Name the parasite shown.
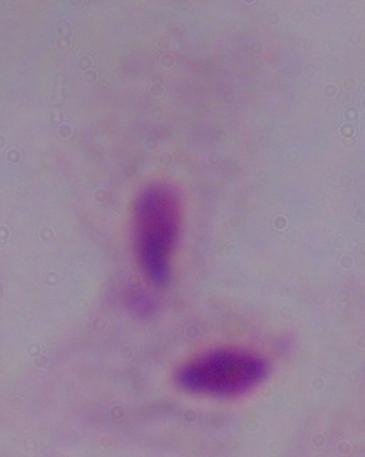
A trichomonad.

{
  "magnification": "1000x",
  "modality": "micrograph"
}